Find the cells and give the type of each one.
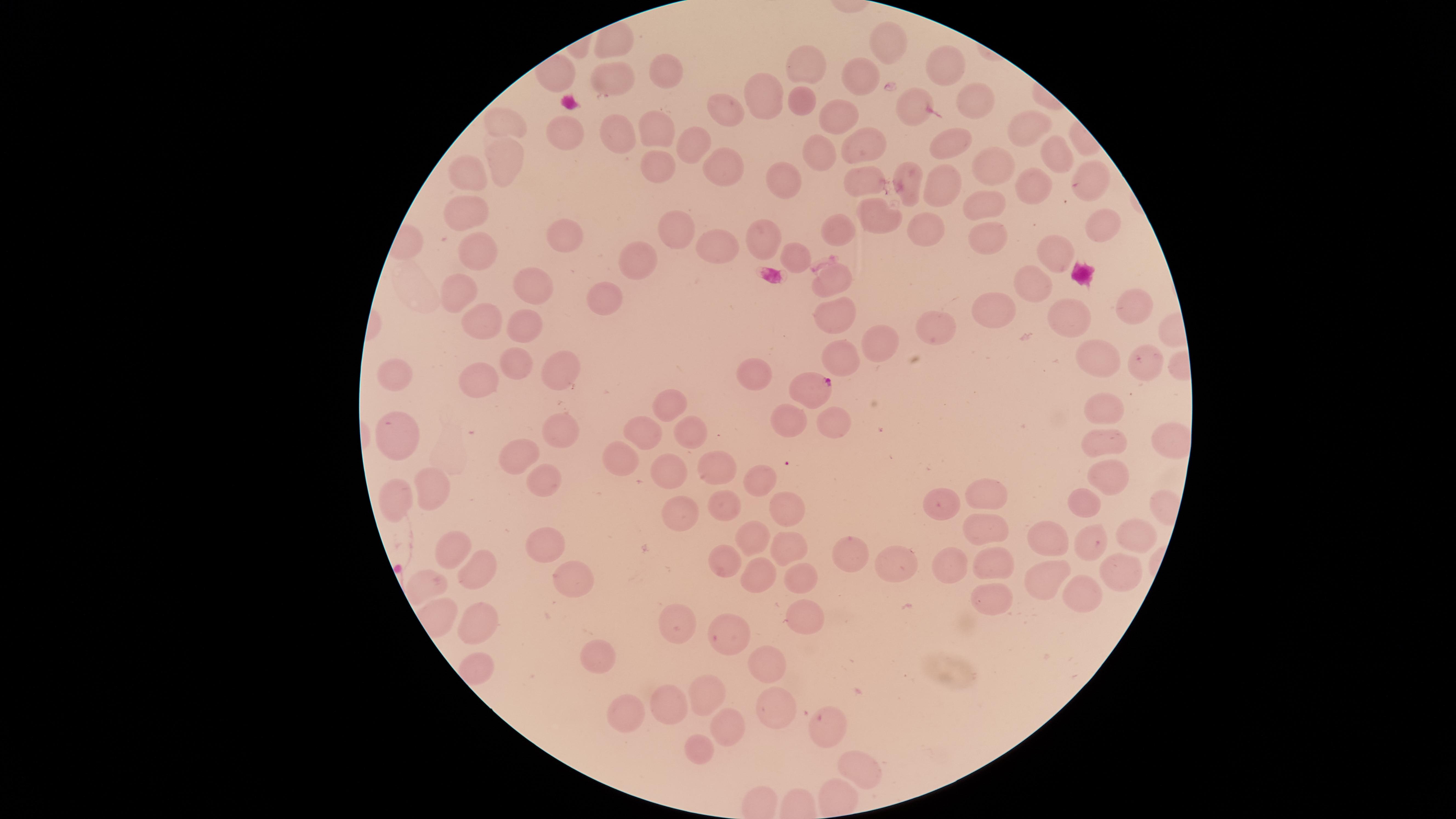
Approximate marker points, in pixels from the top-left corner.
Parasitized red blood cells: (x=814, y=385).
Uninfected red blood cells: (x=889, y=45), (x=808, y=64), (x=948, y=65), (x=660, y=66), (x=862, y=77), (x=617, y=80), (x=763, y=98), (x=974, y=100), (x=804, y=102), (x=912, y=106), (x=725, y=115), (x=842, y=117), (x=506, y=122), (x=1026, y=130), (x=650, y=134), (x=613, y=136), (x=559, y=137), (x=865, y=143), (x=952, y=143), (x=694, y=148), (x=1051, y=154), (x=824, y=155), (x=992, y=157), (x=508, y=164), (x=654, y=164), (x=726, y=164), (x=471, y=169), (x=908, y=175), (x=1090, y=177), (x=867, y=180), (x=782, y=181), (x=1027, y=184), (x=944, y=186), (x=989, y=206), (x=471, y=212), (x=881, y=219), (x=938, y=227), (x=678, y=228), (x=1104, y=228), (x=842, y=229), (x=564, y=233), (x=764, y=233), (x=988, y=236), (x=472, y=247), (x=714, y=249), (x=1057, y=253), (x=645, y=259), (x=795, y=259), (x=1026, y=279), (x=833, y=281), (x=533, y=283), (x=461, y=293), (x=613, y=299), (x=1135, y=305), (x=988, y=312), (x=830, y=313), (x=1075, y=313), (x=476, y=321), (x=524, y=322), (x=937, y=329), (x=876, y=336), (x=843, y=359), (x=1098, y=362), (x=1148, y=362), (x=407, y=365), (x=516, y=366), (x=558, y=369), (x=757, y=375), (x=483, y=383), (x=671, y=403), (x=1106, y=410), (x=789, y=421), (x=834, y=422), (x=562, y=430), (x=648, y=430), (x=395, y=432), (x=1102, y=445), (x=630, y=459), (x=525, y=460), (x=720, y=471), (x=674, y=472), (x=1108, y=475), (x=765, y=477), (x=549, y=481), (x=991, y=488), (x=398, y=493), (x=438, y=493), (x=789, y=504), (x=1082, y=504), (x=943, y=506), (x=724, y=507), (x=683, y=511), (x=980, y=528), (x=750, y=532), (x=1130, y=536), (x=1049, y=539), (x=546, y=543), (x=1091, y=545), (x=457, y=546), (x=783, y=547), (x=858, y=551), (x=993, y=561), (x=725, y=563), (x=952, y=564), (x=898, y=566), (x=479, y=569), (x=1120, y=573), (x=757, y=576), (x=791, y=577), (x=573, y=578), (x=1054, y=579), (x=1077, y=591), (x=992, y=595), (x=483, y=614), (x=801, y=616), (x=673, y=626), (x=730, y=640), (x=600, y=660), (x=766, y=666), (x=705, y=693), (x=668, y=706), (x=772, y=708), (x=631, y=711), (x=726, y=725), (x=828, y=726), (x=698, y=748), (x=863, y=767).
No white blood cells identified.

Species: Plasmodium falciparum. Smartphone photograph through the microscope eyepiece. Single field of view. Thin smear of blood. Giemsa-stained preparation. The visible region is circular. Image is 1456×819 pixels.